Give the position of every Plasmodium falciparum parasite, noting its life-cycle stage.
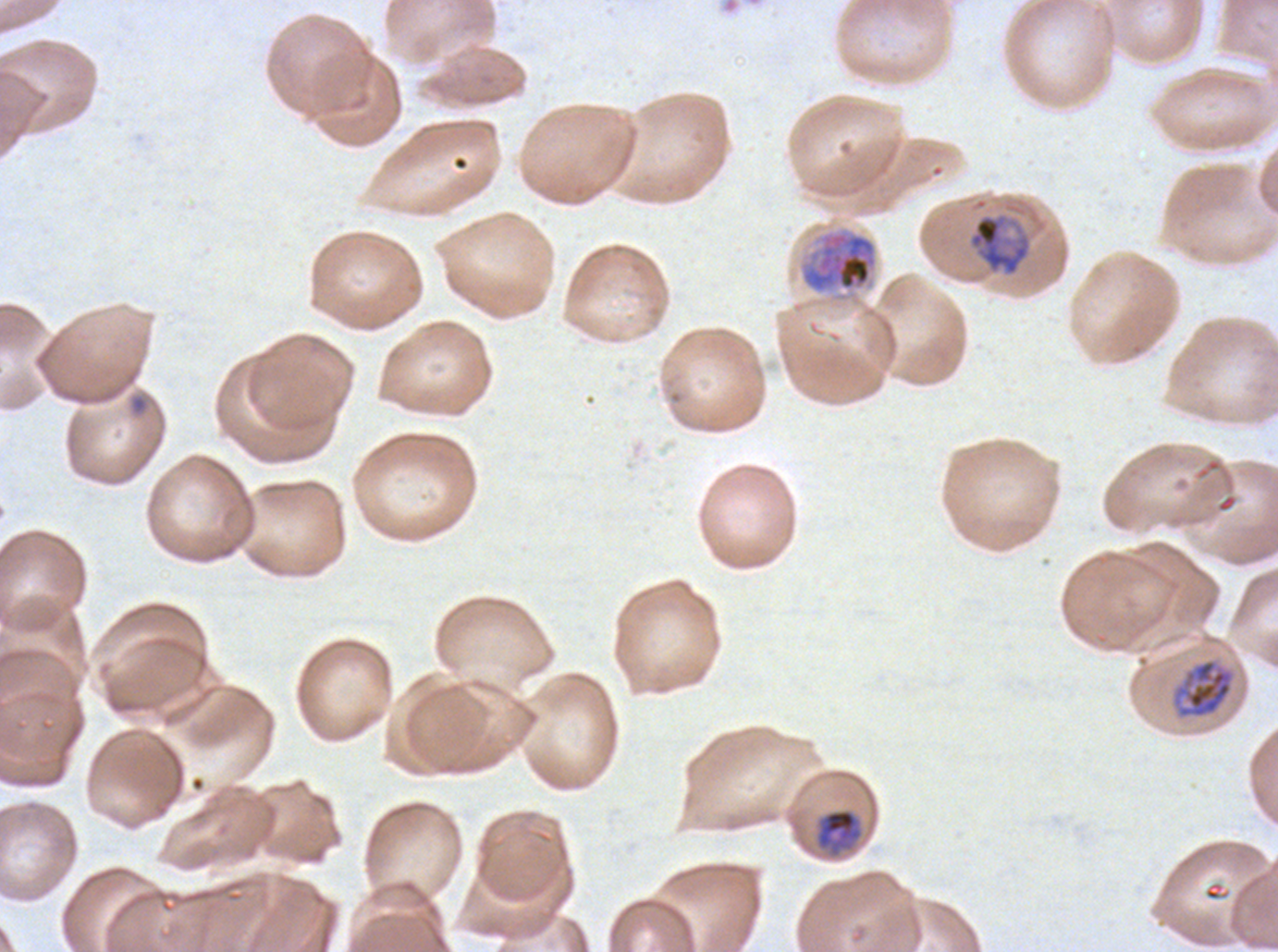

Approximate bounding boxes as [x1, y1, x2, y2] in pixels.
Rings: [130, 396, 147, 412].
Mid trophozoites: [967, 212, 1033, 277], [1172, 658, 1235, 719], [814, 808, 864, 859].
Early schizonts: [798, 226, 879, 295].
No late-ring/early-trophozoite forms, late trophozoites, late schizonts, segmenters, or gametocytes observed.

field of view = one sub-image of a larger composite
life-cycle stages observed = ring, mid trophozoite, early schizont
image size = 1278×952 pixels
preparation = thin blood film
stain = Giemsa
specimen = ex-vivo Plasmodium falciparum culture from a patient in The Gambia, grown for 24 to 48 hours